Classify this cell by malaria status.
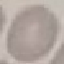

It is uninfected.

Summary:
  - Stain: Giemsa
  - Capture: smartphone camera at the microscope eyepiece
  - Image type: automatically extracted cell patch, resized to 64 × 64 pixels
  - Preparation: thin blood film